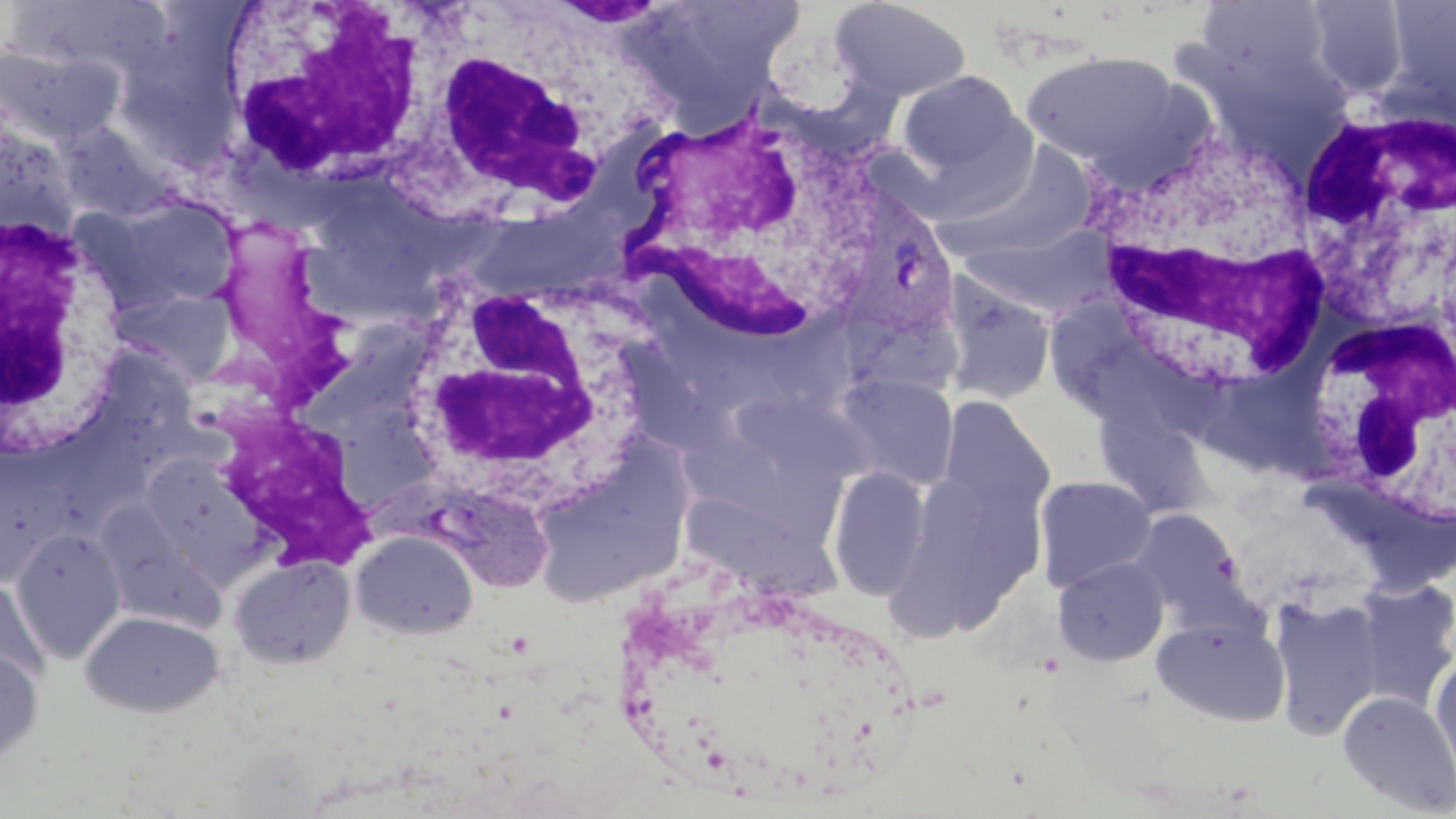
Summary:
  - Coordinate format: approximate bounding boxes as named x1/y1/x2/y2 corners in pixels
  - Plasmodium vivax-infected red blood cell locations: (x1=845, y1=196, x2=959, y2=342)
  - White blood cell locations: (x1=220, y1=1, x2=432, y2=188), (x1=400, y1=43, x2=615, y2=227), (x1=1288, y1=88, x2=1451, y2=301), (x1=610, y1=97, x2=895, y2=351), (x1=1078, y1=120, x2=1336, y2=393), (x1=2, y1=210, x2=127, y2=463), (x1=209, y1=211, x2=371, y2=407), (x1=392, y1=269, x2=660, y2=509), (x1=1305, y1=306, x2=1453, y2=529), (x1=213, y1=405, x2=381, y2=567)
  - Uninfected red blood cell locations: (x1=625, y1=0, x2=806, y2=121), (x1=829, y1=1, x2=972, y2=102), (x1=1304, y1=1, x2=1411, y2=98), (x1=1384, y1=1, x2=1455, y2=109), (x1=5, y1=2, x2=175, y2=85), (x1=1194, y1=3, x2=1335, y2=85), (x1=0, y1=43, x2=121, y2=148), (x1=1020, y1=51, x2=1187, y2=172), (x1=897, y1=70, x2=1023, y2=179), (x1=0, y1=107, x2=80, y2=242), (x1=53, y1=123, x2=175, y2=223), (x1=934, y1=143, x2=1100, y2=265), (x1=91, y1=195, x2=240, y2=312), (x1=959, y1=225, x2=1118, y2=318), (x1=940, y1=277, x2=1056, y2=408), (x1=110, y1=287, x2=237, y2=385), (x1=1047, y1=314, x2=1172, y2=446), (x1=311, y1=324, x2=437, y2=435), (x1=834, y1=372, x2=959, y2=491), (x1=731, y1=397, x2=881, y2=489), (x1=938, y1=398, x2=1055, y2=524), (x1=1099, y1=401, x2=1224, y2=529), (x1=527, y1=441, x2=694, y2=608), (x1=141, y1=452, x2=257, y2=564), (x1=0, y1=464, x2=61, y2=586), (x1=827, y1=467, x2=930, y2=601), (x1=1034, y1=475, x2=1157, y2=592), (x1=897, y1=480, x2=1004, y2=647), (x1=677, y1=497, x2=843, y2=613), (x1=107, y1=502, x2=231, y2=632), (x1=1132, y1=510, x2=1248, y2=623), (x1=11, y1=528, x2=126, y2=662), (x1=351, y1=530, x2=478, y2=640), (x1=227, y1=554, x2=356, y2=670), (x1=1053, y1=557, x2=1169, y2=667), (x1=1351, y1=577, x2=1456, y2=711), (x1=0, y1=578, x2=49, y2=690), (x1=1270, y1=595, x2=1384, y2=739), (x1=79, y1=610, x2=224, y2=718), (x1=1151, y1=615, x2=1290, y2=726), (x1=0, y1=649, x2=43, y2=768), (x1=1429, y1=658, x2=1456, y2=787), (x1=1338, y1=691, x2=1456, y2=816)
  - Slide-level diagnosis: Plasmodium vivax
  - Image size: 1456×819 pixels
  - Modality: optical microscopy
  - Preparation: thin blood smear
  - Field of view: one of a larger specimen
  - Magnification: 1000x
  - Stain: May-Grünwald-Giemsa